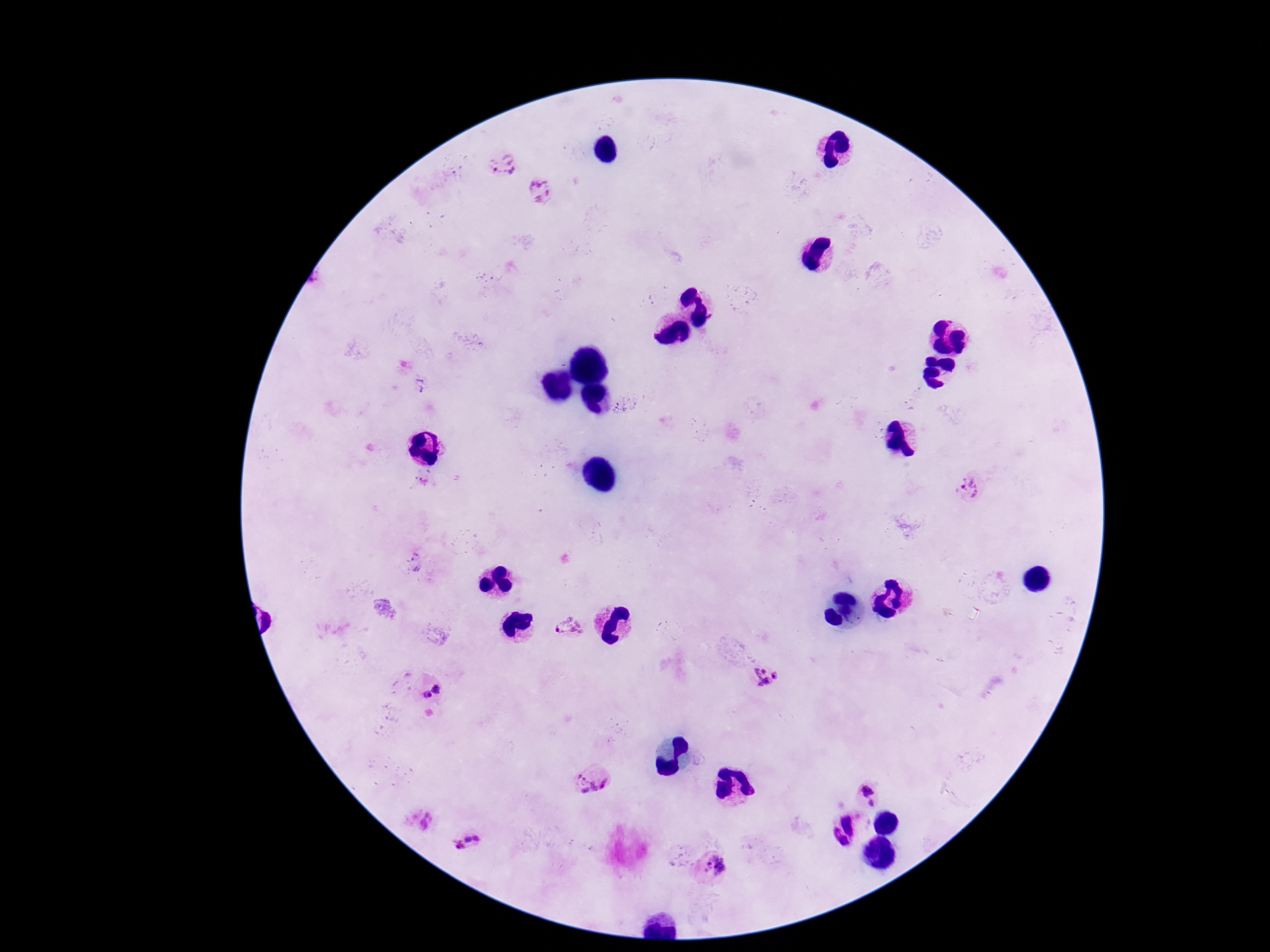
capture = smartphone camera through the microscope eyepiece
stain = Giemsa
Plasmodium parasite locations = approximate centers as [x, y] in pixels: [503, 165], [540, 191], [421, 383], [967, 488], [415, 564], [570, 626], [765, 676], [438, 688], [426, 695], [593, 781], [867, 790], [871, 802], [425, 822], [477, 838], [468, 840], [458, 846], [715, 866]
image size = 1270×952 pixels
field of view = single
preparation = thick peripheral-blood smear
patient malaria status = infected
magnification = 100x